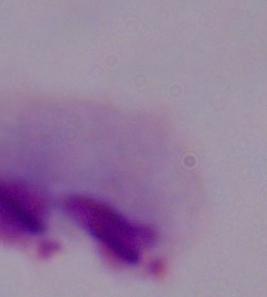
1000x magnification. A trichomonad is shown. Micrograph.